Report the malaria status of this cell.
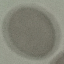

Uninfected.

Giemsa-stained preparation. Cell patch, automatically extracted from a larger field of view and resized to 64 × 64 pixels. Thin blood film. Photographed with a smartphone camera at the microscope eyepiece.